Identify the blood parasite species.
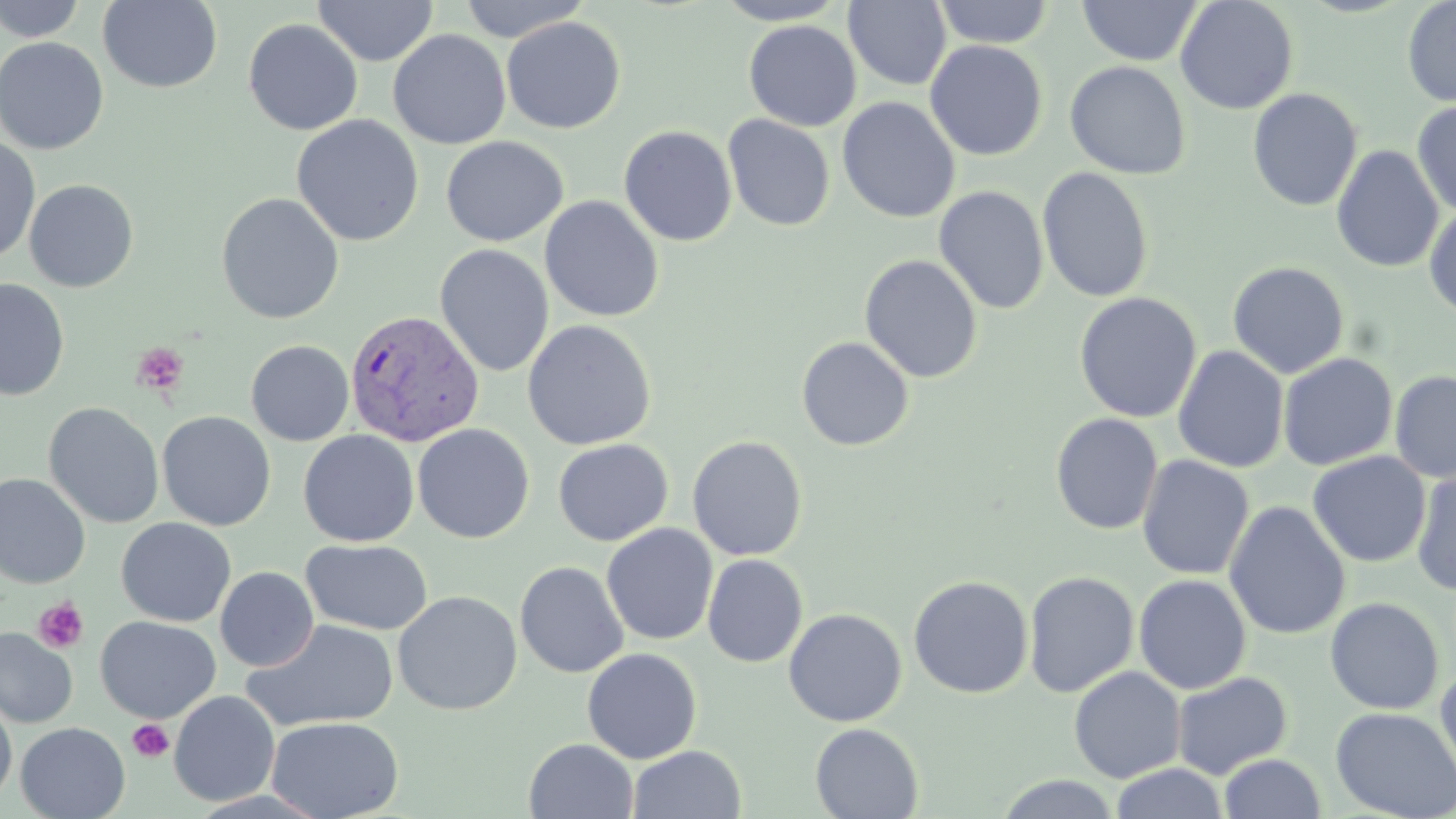
Plasmodium vivax.

Approximate bounding boxes as (x1,y1)-(x2,y2) corner pairs in pixels. Plasmodium vivax-infected red blood cell locations: (344,309)-(484,448). Uninfected red blood cell locations: (0,0)-(89,42), (312,0)-(439,67), (455,0)-(592,42), (712,0)-(852,25), (933,0)-(1055,48), (1175,0)-(1299,115), (1402,0)-(1456,107), (97,1)-(223,93), (843,1)-(952,91), (1077,1)-(1203,67), (501,16)-(626,134), (243,19)-(363,135), (743,19)-(862,132), (388,29)-(511,150), (0,36)-(109,155), (925,40)-(1047,161), (1064,60)-(1191,180), (1247,88)-(1363,212), (837,96)-(960,224), (1411,100)-(1456,217), (291,114)-(425,246), (722,114)-(835,232), (618,125)-(738,246), (0,135)-(41,264), (440,135)-(569,248), (1332,144)-(1445,273), (1037,166)-(1155,303), (23,179)-(139,292), (933,185)-(1049,314), (215,192)-(345,324), (539,195)-(664,323), (1423,204)-(1456,322), (435,244)-(555,378), (859,254)-(983,384), (1227,261)-(1349,378), (0,279)-(70,401), (1074,292)-(1202,423), (522,319)-(657,451), (795,336)-(915,451), (245,340)-(354,446), (1172,346)-(1289,474), (1277,352)-(1398,471), (1390,370)-(1456,483), (42,402)-(164,529), (156,410)-(276,531), (1050,413)-(1163,535), (412,424)-(535,543), (298,429)-(419,547), (687,435)-(808,561), (553,438)-(674,546), (1307,451)-(1431,568), (1136,455)-(1254,580), (1411,468)-(1456,597), (0,473)-(91,588), (1223,501)-(1351,640), (116,517)-(236,627), (601,523)-(718,646), (301,538)-(433,635), (703,554)-(807,668), (514,561)-(628,679), (214,567)-(319,672), (1023,570)-(1140,698), (908,574)-(1034,698), (1134,574)-(1251,694), (392,590)-(523,716), (1325,596)-(1445,715), (783,607)-(907,727), (95,616)-(221,723), (242,619)-(397,733), (0,626)-(78,729), (581,648)-(702,764), (1435,665)-(1456,792), (1068,666)-(1186,783), (1171,671)-(1292,780), (168,690)-(280,807), (0,696)-(17,809), (1330,706)-(1456,819), (267,716)-(404,819), (15,722)-(130,819), (810,723)-(923,818), (523,738)-(639,819), (627,745)-(746,819), (1219,753)-(1327,819), (1109,763)-(1229,819), (994,774)-(1123,818). Platelet locations: (132,343)-(189,396), (33,597)-(88,653), (127,719)-(174,763). Optical microscopy. Single field of view. Thin blood film. 1000x magnification. May-Grünwald-Giemsa-stained preparation. Image is 1456×819 pixels.